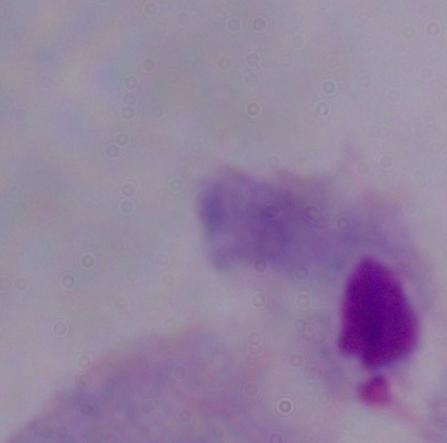
modality = photomicrograph
identification = trichomonad
magnification = 1000x